State which parasite is depicted.
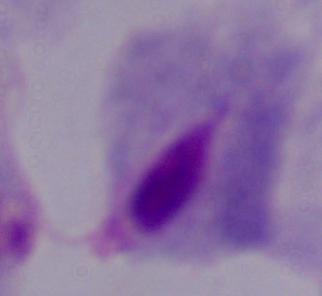
A trichomonad.

magnification: 1000x
modality: micrograph